Identify the parasite.
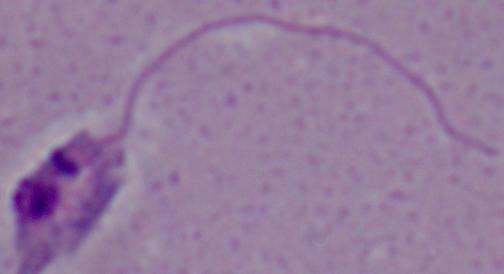

This is Leishmania.

Micrograph. Captured at 1000x magnification.